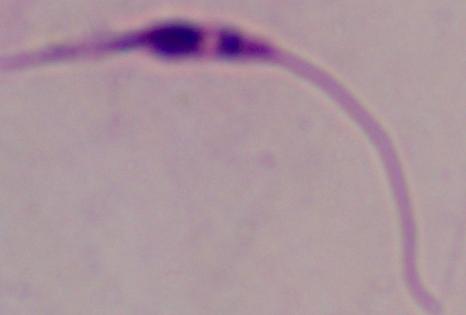

{
  "modality": "photomicrograph",
  "magnification": "1000x",
  "identification": "Leishmania"
}